Report the malaria status of this cell.
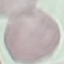

It is uninfected.

Summary:
  - Preparation: thin blood film
  - Stain: Giemsa
  - Capture: smartphone through the microscope eyepiece
  - Image type: cell patch, automatically extracted from a larger field of view and resized to 64 × 64 pixels